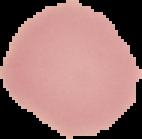
Summary:
  - Image size: 142×139 pixels
  - Preparation: thin blood smear
  - Image type: segmented cell region with the area outside set to black
  - Result: no Plasmodium parasites seen